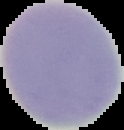

image size = 124×130 pixels
preparation = thin blood film
image type = segmented cell region with the area outside set to black
malaria status = uninfected